Assess this cell for malaria.
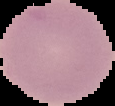

Uninfected.

Summary:
  - Image size: 115×106 pixels
  - Preparation: thin blood smear
  - Image type: segmented cell region with the area outside set to black